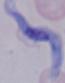

magnification = 1000x
modality = photomicrograph
identification = trypanosome